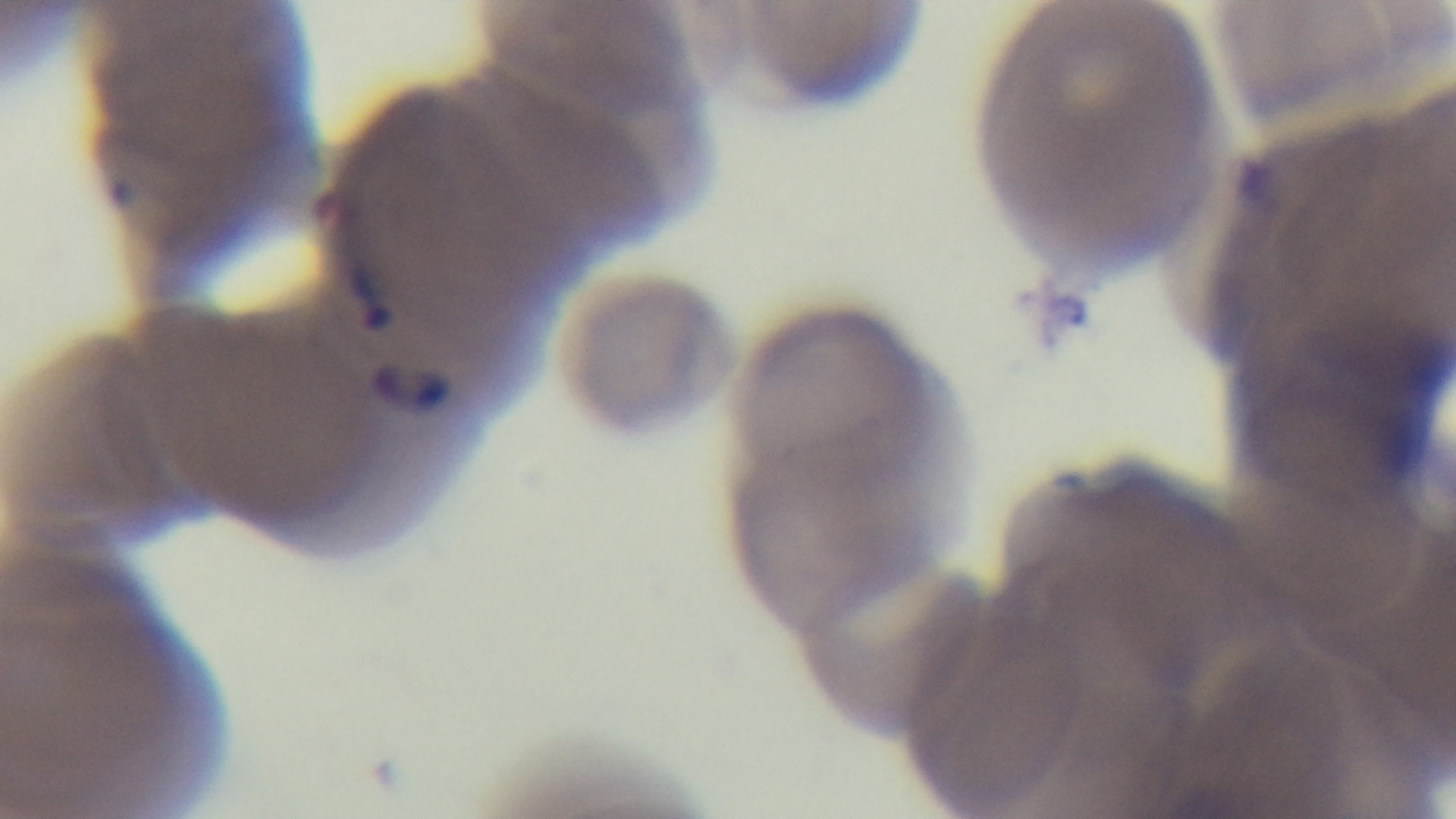

field of view = one from the slide
modality = light microscopy
preparation = thin
capture = mounted 4K digital camera
malaria status = infected
objective = 100x oil immersion
stain = Giemsa